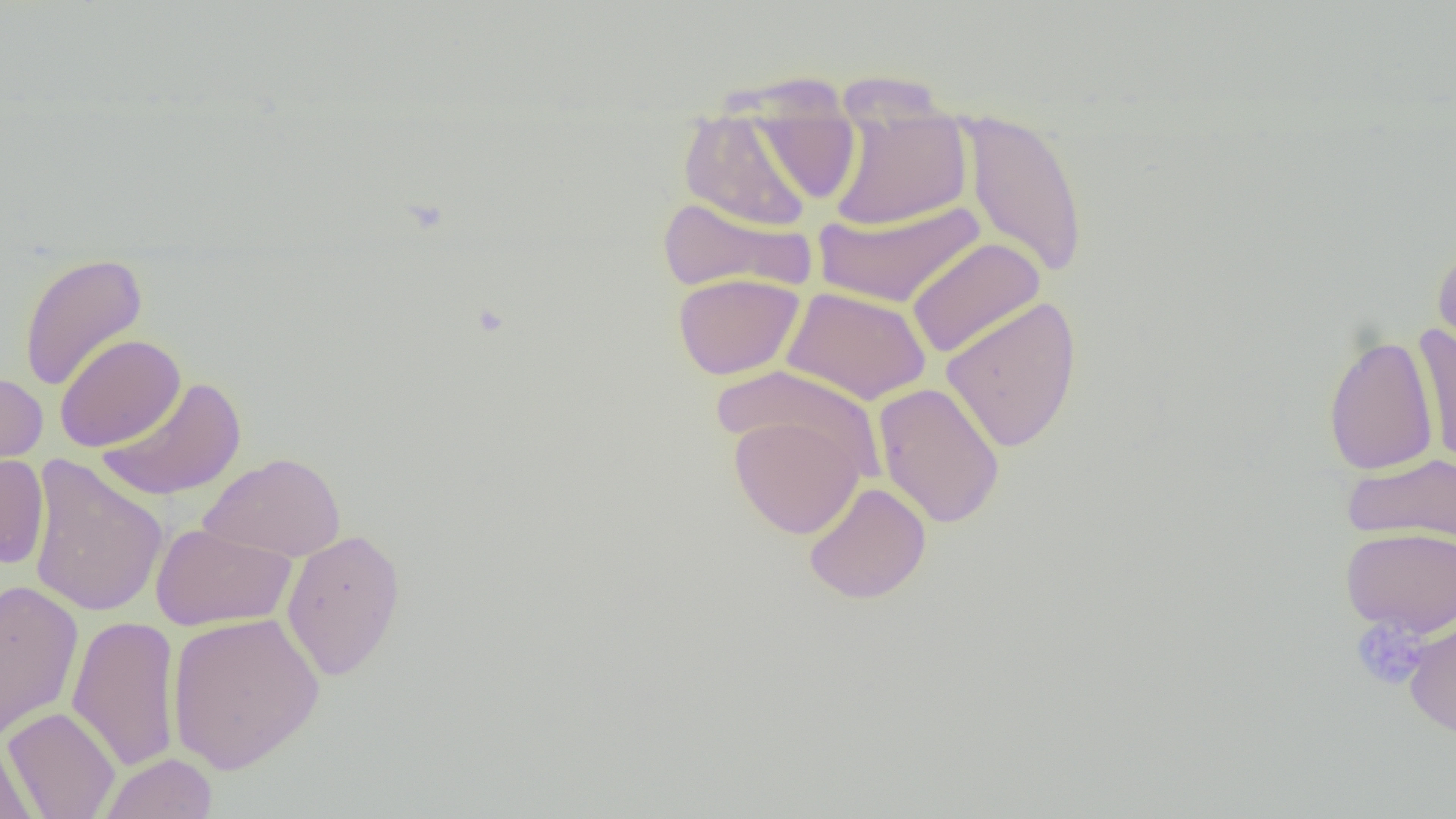 Approximate bounding boxes as (x1,y1)-(x2,y2) corner pairs in pixels. Platelet locations: (1351,617)-(1428,690). Uninfected red blood cell locations: (739,84)-(865,207), (826,96)-(972,232), (960,107)-(1089,280), (679,111)-(815,232), (656,196)-(813,295), (813,199)-(985,308), (906,237)-(1045,359), (1431,244)-(1456,361), (18,252)-(148,393), (673,272)-(805,380), (782,286)-(932,405), (940,296)-(1083,454), (1413,324)-(1456,470), (54,333)-(185,452), (1323,334)-(1438,475), (713,365)-(886,480), (0,372)-(48,475), (95,376)-(248,502), (874,382)-(1005,529), (729,413)-(865,540), (199,452)-(345,561), (0,453)-(49,569), (1343,454)-(1456,545), (26,455)-(168,618), (804,481)-(931,605), (150,523)-(297,631), (1340,526)-(1456,636), (281,528)-(406,681), (0,581)-(83,741), (166,611)-(325,774), (1402,613)-(1456,738), (67,616)-(182,772), (4,706)-(121,818), (0,735)-(37,819), (98,752)-(218,819). Slide-level diagnosis: no evidence of blood parasites. One field of a larger specimen. Thin blood smear. 1000x magnification. Light microscopy. Image is 1456×819 pixels.